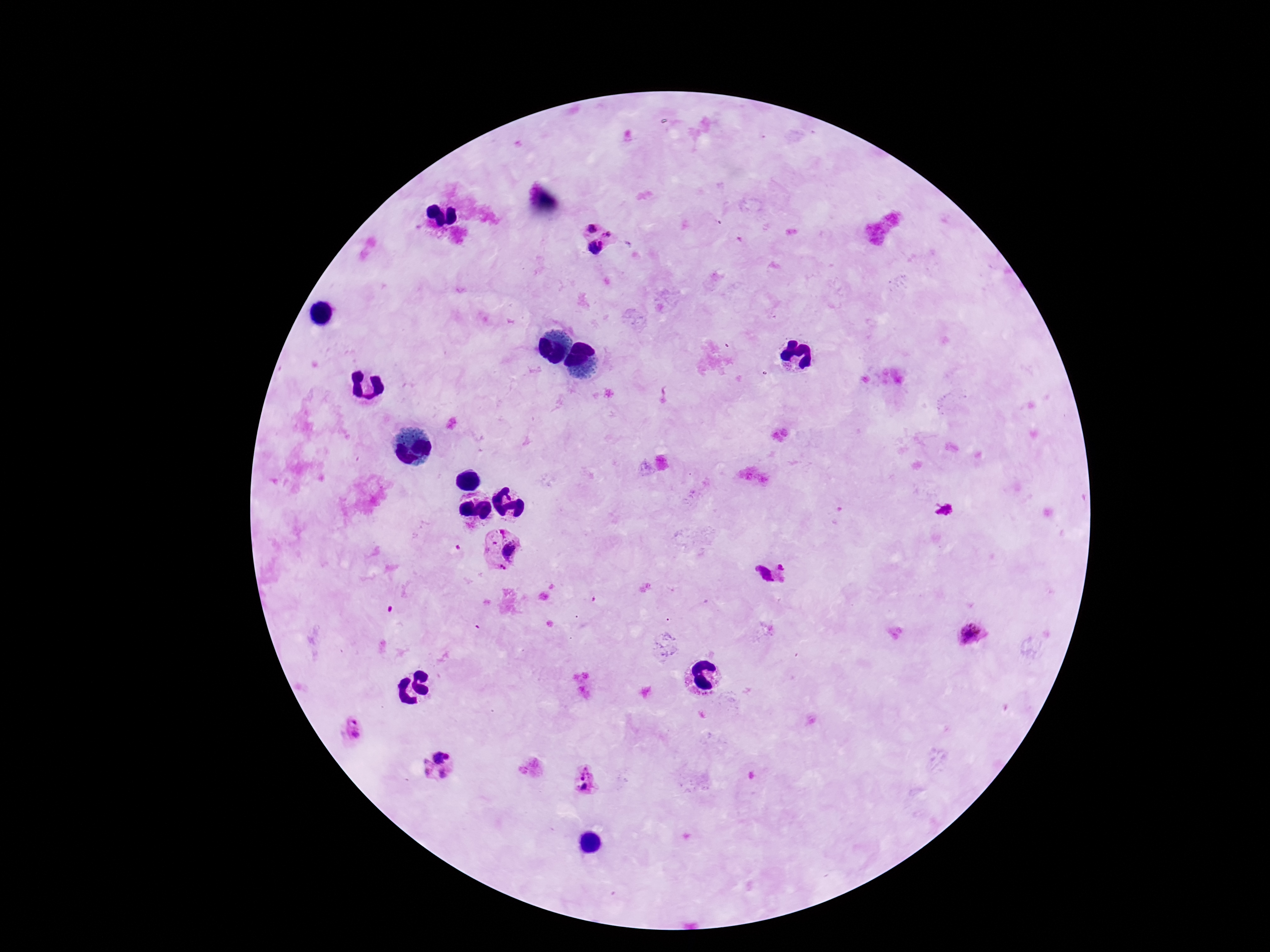
Approximate object centers, in pixels from the top-left corner.
Summary:
  - Plasmodium parasite locations: (x=592, y=227), (x=610, y=233), (x=596, y=248), (x=504, y=552), (x=782, y=567), (x=763, y=575), (x=970, y=633), (x=353, y=728), (x=441, y=756), (x=427, y=768), (x=585, y=773), (x=443, y=774), (x=585, y=787)
  - Patient malaria status: positive
  - Image size: 1270×952 pixels
  - Preparation: thick peripheral-blood smear
  - Magnification: 100x
  - Stain: Giemsa
  - Field of view: single
  - Capture: smartphone camera through the microscope eyepiece